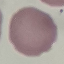
Malaria status: uninfected. Thin blood film. Giemsa stain. Acquired by smartphone through the microscope eyepiece. Cell patch, automatically extracted from a larger field of view and resized to 64 × 64 pixels.